Classify this cell by malaria status.
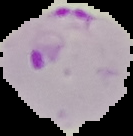

It is parasitized.

Cell region segmented out of the field of view; the surrounding area is masked to black. Image is 133×136 pixels. From a thin blood film.